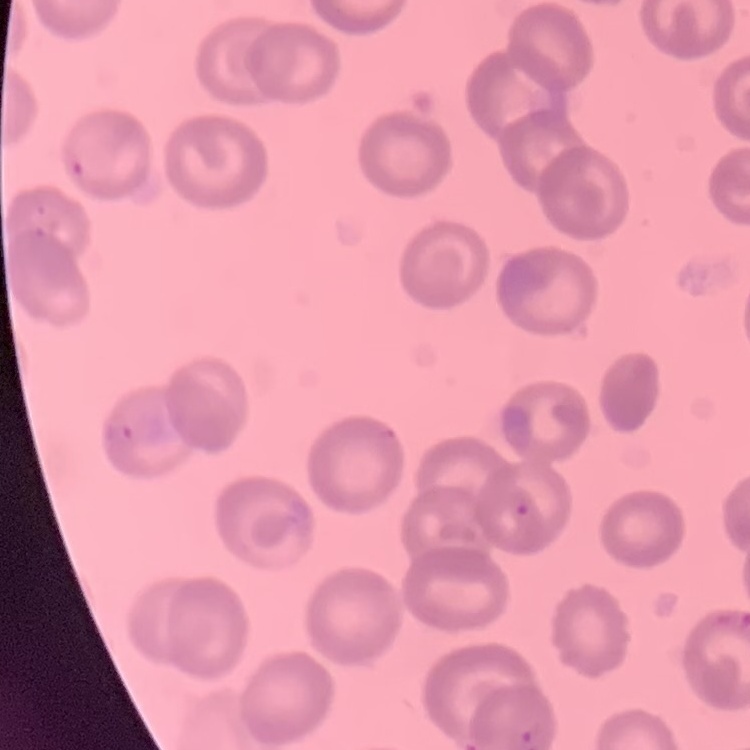 The red blood cells exhibit no rouleaux formation. Thin blood smear. Stained with either Field's or Giemsa. Square crop of a larger photomicrograph.